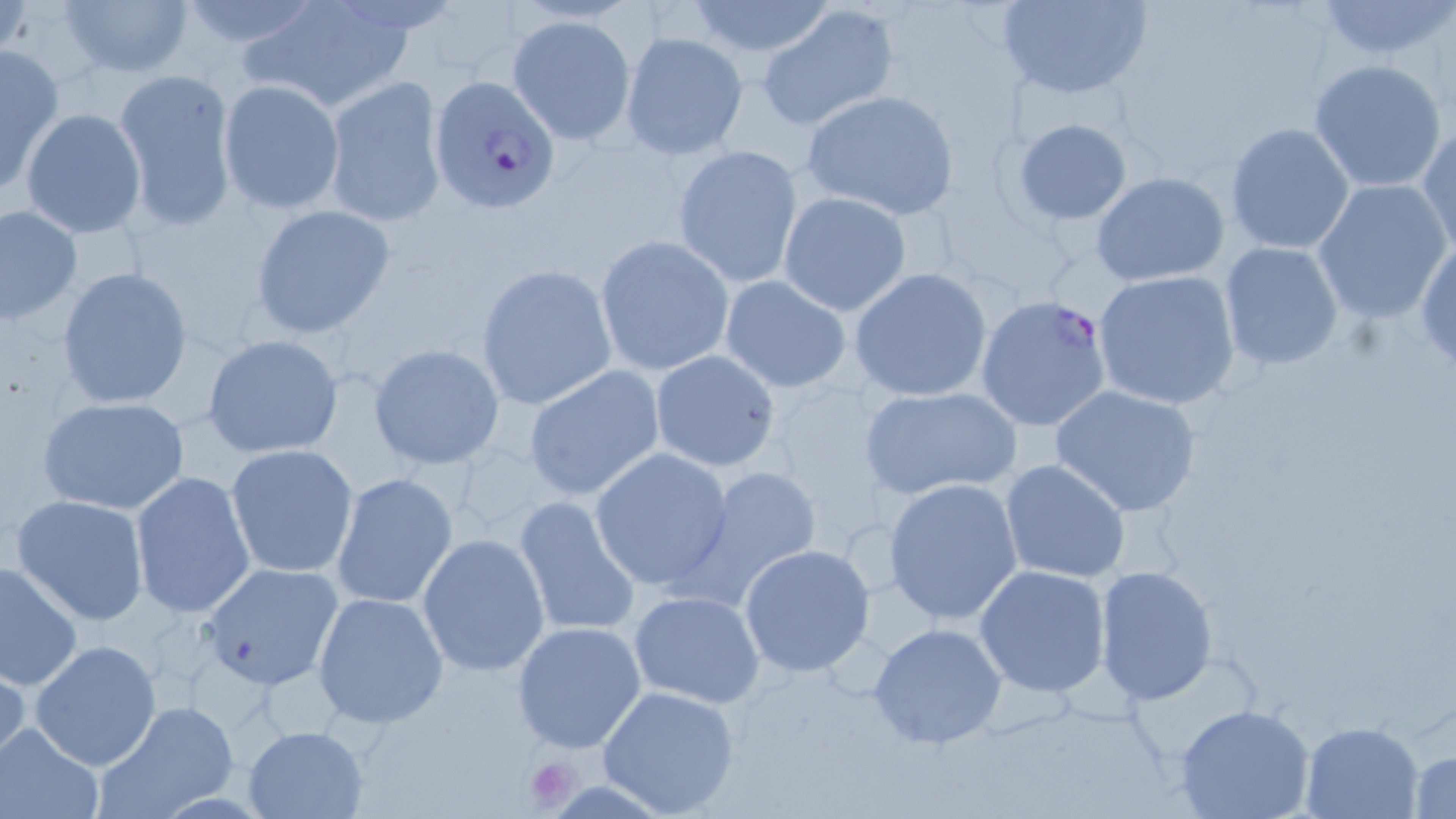
{
  "slide_level_diagnosis": "Plasmodium falciparum",
  "field_of_view": "single",
  "modality": "optical microscopy",
  "uninfected_red_blood_cell_locations": "approximate bounding boxes as [x1, y1, x2, y2] in pixels: [59, 0, 194, 80], [172, 0, 323, 52], [994, 0, 1154, 99], [243, 1, 414, 112], [682, 1, 838, 59], [1313, 1, 1455, 61], [756, 4, 898, 130], [506, 14, 637, 144], [619, 31, 748, 160], [0, 43, 65, 194], [1307, 58, 1449, 194], [112, 68, 238, 228], [324, 75, 447, 227], [219, 80, 345, 214], [800, 91, 959, 219], [20, 108, 146, 237], [1012, 118, 1133, 225], [1224, 122, 1356, 254], [1416, 123, 1455, 259], [671, 144, 805, 290], [1089, 172, 1232, 287], [1311, 179, 1453, 323], [778, 191, 911, 316], [248, 203, 397, 340], [0, 205, 82, 324], [594, 235, 734, 376], [1414, 237, 1456, 374], [1218, 240, 1345, 370], [475, 264, 617, 410], [57, 266, 194, 411], [849, 268, 993, 402], [1092, 269, 1242, 410], [718, 276, 851, 393], [202, 334, 344, 458], [367, 343, 504, 469], [649, 349, 780, 472], [521, 365, 666, 503], [861, 384, 1021, 500], [1050, 384, 1204, 518], [38, 396, 191, 516], [225, 445, 361, 580], [589, 447, 735, 591], [1000, 458, 1132, 586], [676, 466, 824, 611], [130, 471, 255, 620], [330, 473, 458, 610], [882, 477, 1026, 625], [11, 493, 150, 626], [513, 494, 641, 639], [416, 532, 550, 676], [738, 545, 875, 678], [0, 558, 82, 692], [199, 562, 344, 691], [974, 563, 1111, 697], [1093, 565, 1218, 704], [627, 590, 766, 710], [312, 592, 449, 728], [511, 621, 649, 755], [867, 623, 1008, 750], [29, 639, 161, 771], [0, 654, 28, 773], [598, 685, 742, 816], [93, 701, 238, 817], [1173, 702, 1315, 819], [1299, 721, 1423, 818], [1, 725, 102, 818], [243, 725, 368, 817], [1407, 744, 1456, 818]",
  "platelet_locations": "approximate bounding boxes as [x1, y1, x2, y2] in pixels: [525, 756, 580, 812]",
  "plasmodium_falciparum_infected_red_blood_cell_locations": "approximate bounding boxes as [x1, y1, x2, y2] in pixels: [428, 73, 561, 215], [977, 294, 1113, 432]",
  "image_size": "1456×819 pixels",
  "magnification": "1000x",
  "stain": "May-Grünwald-Giemsa",
  "preparation": "thin blood smear"
}